Report the malaria status of this cell.
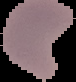

Parasitized.

Image is 76×82 pixels. From a thin blood smear. Cell region segmented out of the field of view; the surrounding area is masked to black.